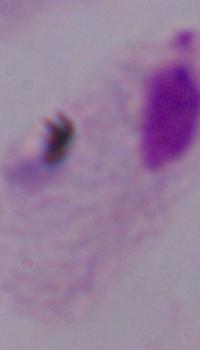

modality = micrograph
identification = trichomonad
magnification = 1000x